Identify the cell.
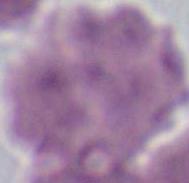
This is an erythrocyte.

modality: micrograph
magnification: 1000x